Give the preparation type.
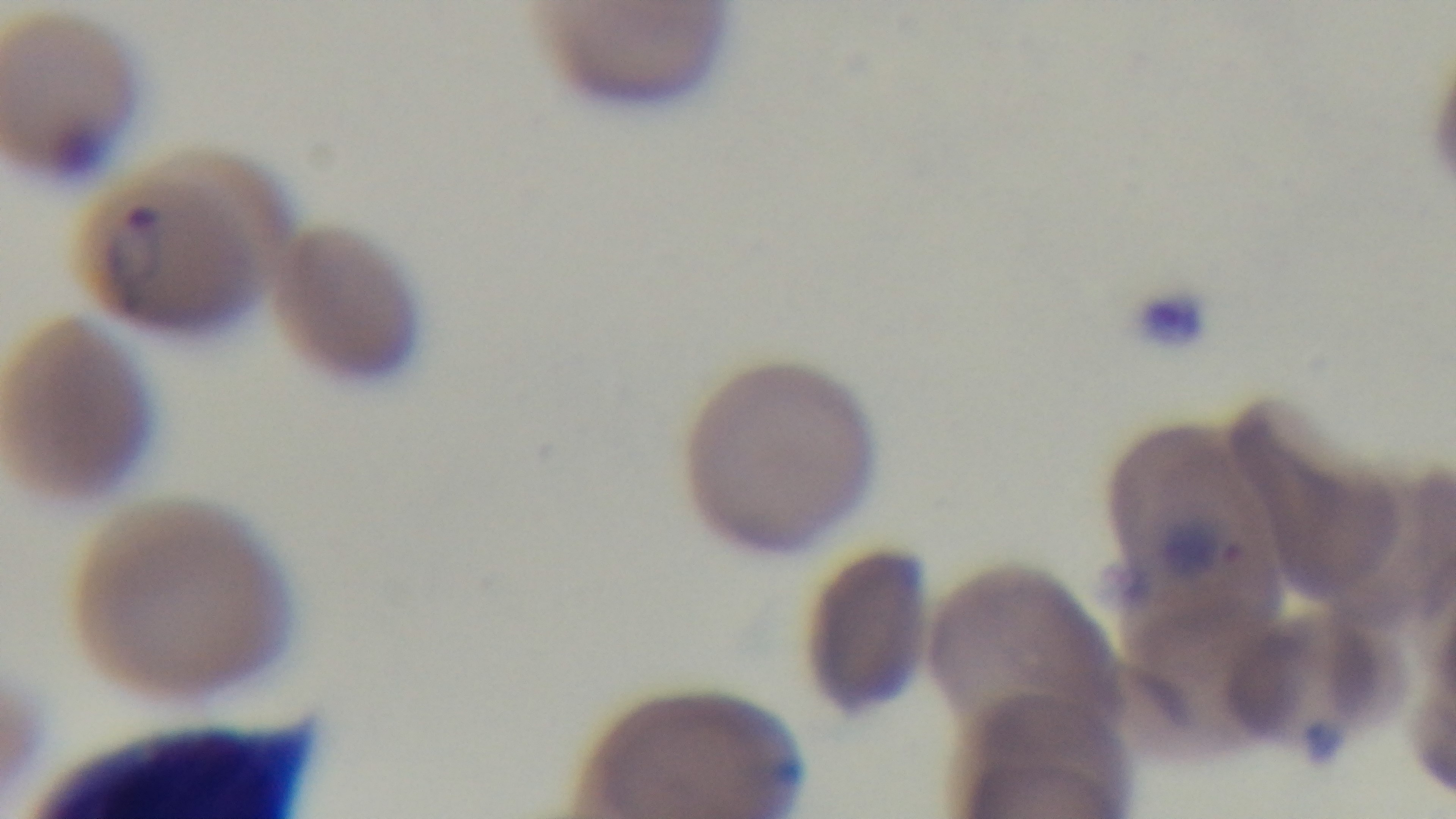

It is a thin blood film.

Oil-immersion objective, 100x. Light microscopy. Mounted 4K digital camera. One field from the slide. Malaria status: positive. Giemsa-stained.